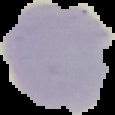

Cell region segmented out of the field of view; the surrounding area is masked to black. From a thin blood smear. Result: no Plasmodium parasites detected. Image is 115×115 pixels.